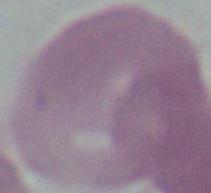

1000x magnification. An erythrocyte is shown. Micrograph.